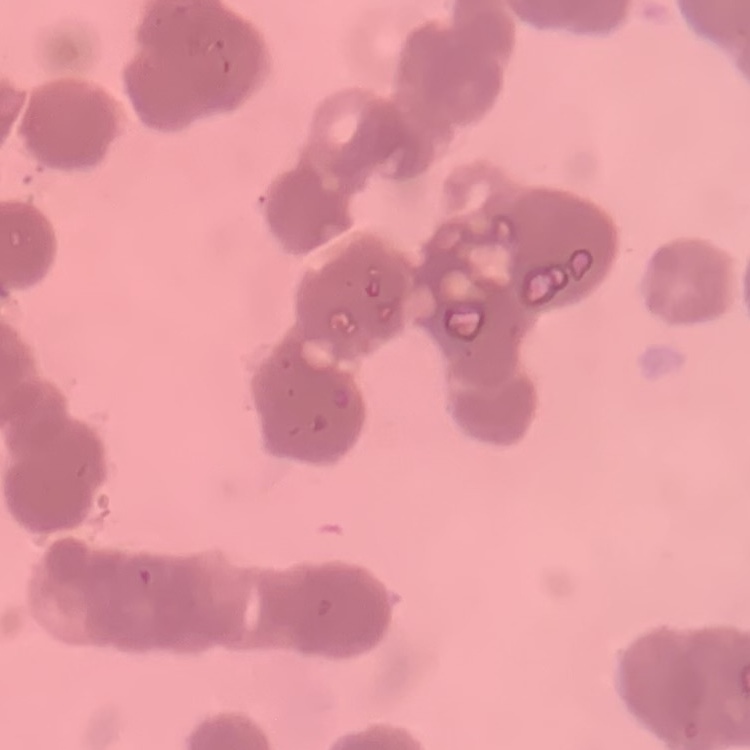

red blood cell morphology = rouleaux formation
stain = Field's or Giemsa
preparation = thin blood smear
image type = square crop of a larger photomicrograph